Outline each Plasmodium falciparum-infected red blood cell.
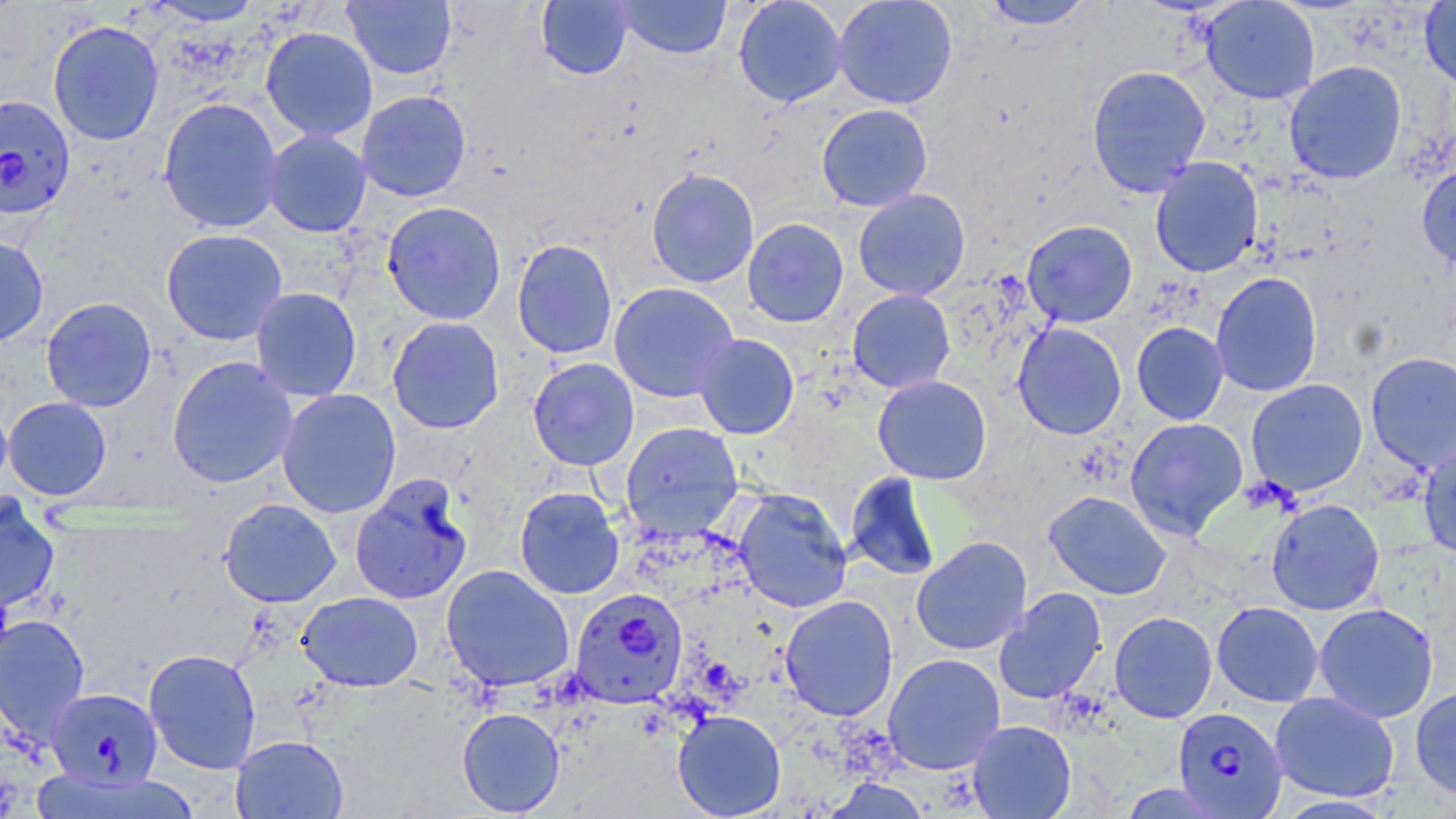
Approximate bounding boxes as (x1, y1, x2, y2) in pixels.
Plasmodium falciparum-infected red blood cells: (0, 94, 75, 221), (569, 588, 688, 709), (47, 687, 162, 789), (1172, 707, 1288, 818).

{
  "slide_level_diagnosis": "Plasmodium falciparum",
  "stain": "May-Grünwald-Giemsa",
  "preparation": "thin blood smear",
  "modality": "light microscopy",
  "uninfected_red_blood_cell_locations": "approximate bounding boxes as (x1, y1, x2, y2) in pixels: (342, 0, 456, 80), (536, 0, 634, 80), (615, 0, 731, 59), (733, 0, 848, 107), (832, 0, 958, 109), (981, 0, 1095, 30), (1201, 0, 1320, 104), (143, 1, 267, 27), (1419, 1, 1456, 89), (47, 19, 165, 146), (260, 25, 378, 142), (1284, 60, 1407, 184), (1086, 64, 1211, 197), (356, 90, 472, 202), (157, 97, 284, 234), (816, 103, 933, 212), (263, 129, 373, 237), (1149, 157, 1263, 277), (1417, 163, 1456, 271), (645, 167, 760, 289), (852, 189, 970, 300), (382, 201, 507, 325), (742, 218, 849, 327), (1022, 219, 1137, 327), (160, 228, 288, 345), (0, 233, 49, 347), (512, 239, 617, 359), (1210, 271, 1323, 397), (608, 281, 739, 403), (250, 286, 362, 402), (846, 289, 956, 394), (40, 297, 157, 412), (387, 316, 505, 434), (1012, 322, 1127, 440), (1131, 322, 1229, 425), (693, 333, 799, 439), (1365, 351, 1456, 474), (167, 355, 298, 488), (527, 357, 639, 470), (872, 374, 992, 484), (1245, 378, 1368, 496), (276, 388, 401, 518), (0, 396, 13, 497), (3, 396, 112, 500), (1124, 417, 1248, 539), (621, 422, 743, 540), (1418, 442, 1456, 561), (844, 471, 942, 581), (350, 474, 473, 605), (514, 486, 625, 600), (732, 488, 852, 613), (1044, 490, 1172, 599), (0, 497, 60, 612), (219, 498, 341, 607), (1266, 498, 1385, 615), (911, 535, 1032, 655), (441, 564, 574, 692), (994, 587, 1107, 705), (297, 591, 423, 692), (779, 594, 899, 721), (1211, 601, 1324, 707), (1313, 603, 1439, 723), (1109, 611, 1217, 723), (0, 613, 90, 744), (144, 648, 262, 774), (883, 652, 1005, 774), (1410, 686, 1456, 798), (1269, 691, 1400, 802), (457, 707, 565, 817), (672, 710, 786, 818), (968, 720, 1076, 818), (230, 735, 348, 818)",
  "image_size": "1456×819 pixels",
  "field_of_view": "one of a larger specimen",
  "magnification": "1000x"
}